State the blood parasite species.
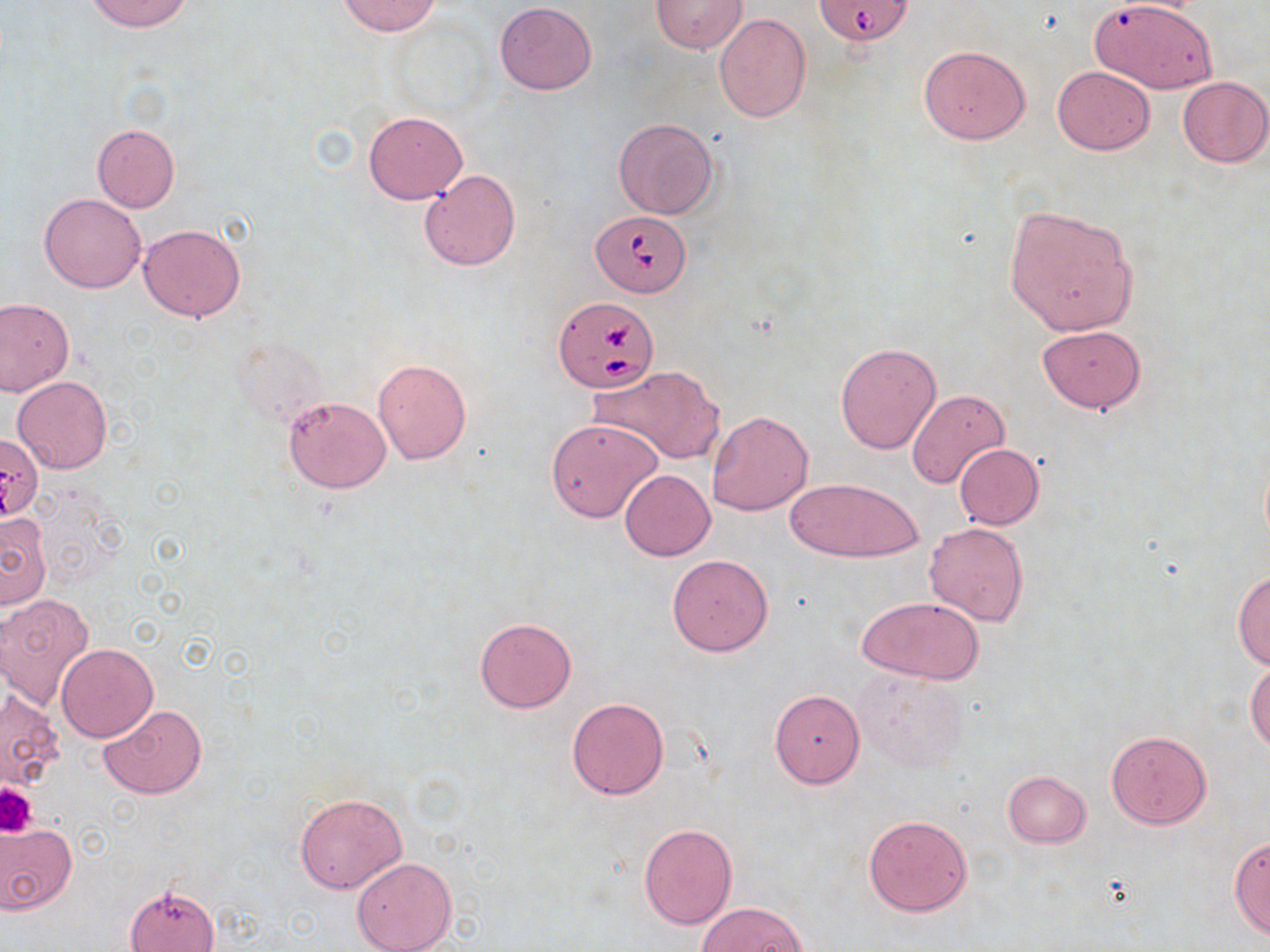
Babesia divergens.

Summary:
  - Coordinate format: approximate bounding boxes as (x1, y1, x2, y2) in pixels
  - Platelet locations: (0, 782, 36, 836)
  - Uninfected red blood cell locations: (85, 0, 194, 33), (337, 0, 442, 36), (652, 0, 747, 54), (1090, 1, 1222, 96), (494, 3, 597, 96), (714, 13, 811, 122), (918, 44, 1031, 144), (1052, 66, 1156, 155), (1177, 76, 1270, 168), (364, 112, 468, 204), (612, 118, 719, 220), (91, 123, 180, 212), (419, 169, 521, 272), (39, 192, 146, 293), (1003, 206, 1138, 336), (139, 223, 245, 322), (0, 299, 74, 395), (1037, 325, 1145, 413), (835, 343, 941, 454), (372, 357, 473, 464), (586, 366, 724, 465), (12, 376, 112, 474), (906, 387, 1009, 487), (283, 395, 392, 493), (707, 410, 813, 516), (546, 418, 663, 523), (954, 444, 1044, 530), (620, 469, 715, 560), (785, 476, 923, 563), (0, 511, 52, 611), (924, 522, 1029, 627), (667, 554, 773, 657), (1232, 570, 1270, 669), (1, 594, 94, 710), (856, 596, 987, 684), (474, 617, 577, 713), (56, 643, 157, 741), (1246, 662, 1270, 752), (853, 670, 967, 773), (1, 689, 65, 793), (769, 689, 865, 787), (566, 697, 670, 801), (98, 705, 207, 799), (1107, 731, 1211, 830), (1002, 770, 1090, 848), (295, 792, 406, 893), (862, 814, 974, 917), (0, 822, 77, 914), (638, 823, 737, 929), (1228, 837, 1270, 940), (351, 856, 456, 952), (125, 884, 218, 952), (698, 903, 806, 952)
  - Babesia divergens-infected red blood cell locations: (816, 0, 913, 46), (590, 209, 691, 297), (554, 297, 658, 393), (0, 434, 43, 522)
  - Field of view: one of a larger specimen
  - Magnification: 1000x
  - Modality: light microscopy
  - Stain: May-Grünwald-Giemsa
  - Preparation: thin blood film
  - Image size: 1270×952 pixels